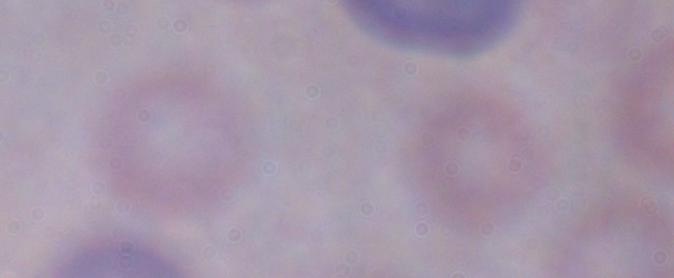

magnification = 1000x
identification = trypanosome
modality = photomicrograph